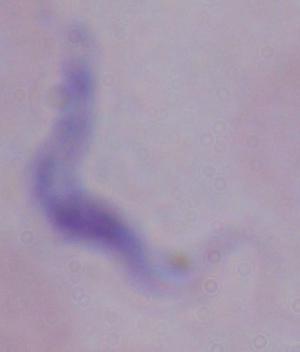 Photomicrograph. 1000x magnification. A trypanosome is shown.